Assess this cell for malaria.
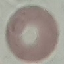

Uninfected.

Summary:
  - Capture: smartphone camera at the microscope eyepiece
  - Stain: Giemsa
  - Image type: automatically extracted cell patch, resized to 64 × 64 pixels
  - Preparation: thin smear